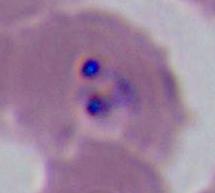
Captured at either 400x or 1000x magnification. A Plasmodium parasite is seen. Photomicrograph.